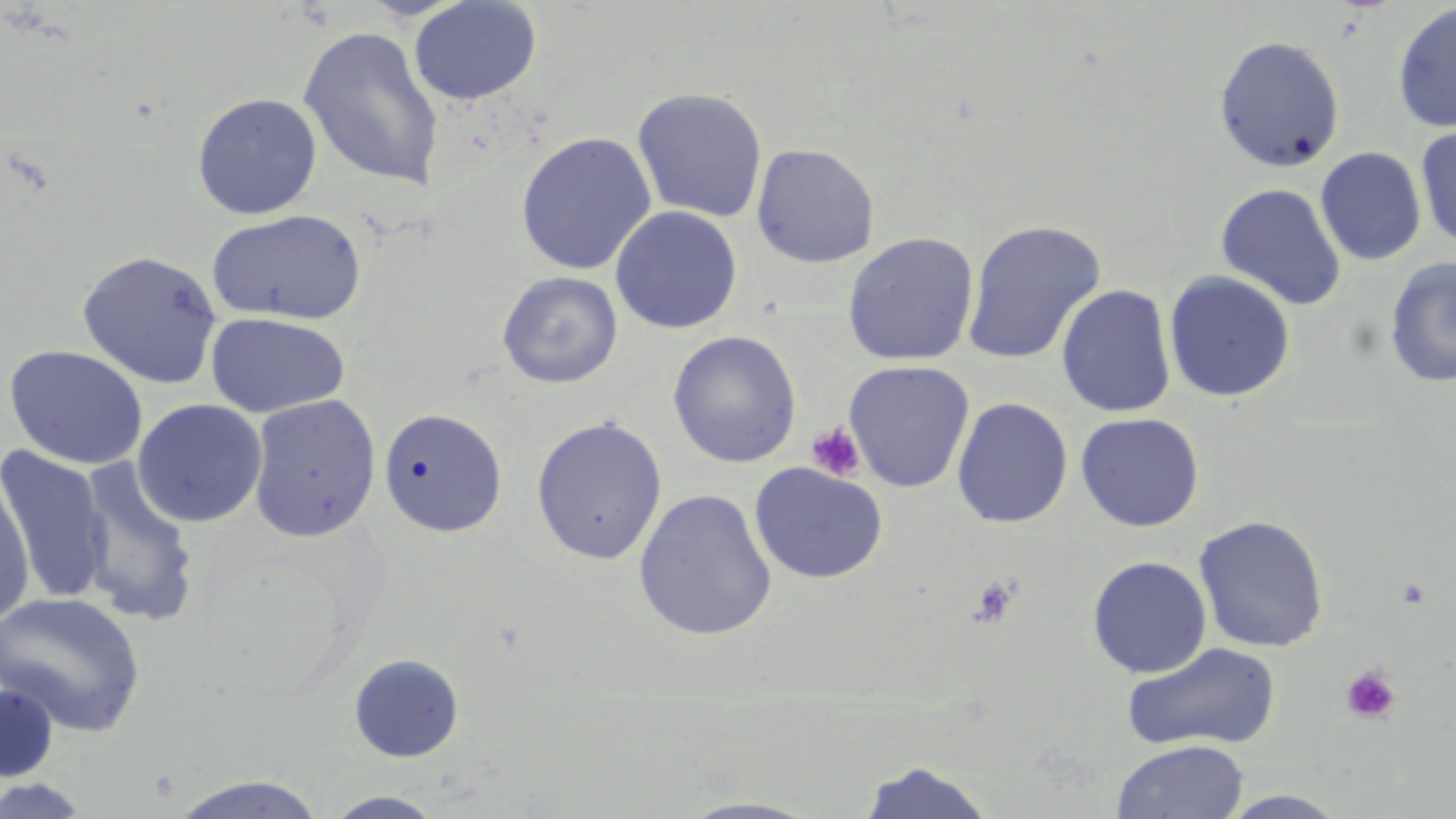

Summary:
  - Coordinate format: approximate bounding boxes as named x1/y1/x2/y2 corners in pixels
  - Uninfected red blood cell locations: (x1=409, y1=0, x2=541, y2=105), (x1=1392, y1=3, x2=1456, y2=134), (x1=297, y1=26, x2=445, y2=192), (x1=1214, y1=35, x2=1345, y2=172), (x1=632, y1=87, x2=768, y2=223), (x1=192, y1=93, x2=322, y2=219), (x1=1414, y1=124, x2=1456, y2=249), (x1=516, y1=132, x2=656, y2=275), (x1=751, y1=143, x2=880, y2=268), (x1=1315, y1=147, x2=1426, y2=266), (x1=1215, y1=182, x2=1346, y2=310), (x1=610, y1=206, x2=742, y2=333), (x1=207, y1=210, x2=367, y2=326), (x1=961, y1=219, x2=1107, y2=365), (x1=842, y1=232, x2=980, y2=365), (x1=77, y1=250, x2=223, y2=389), (x1=1385, y1=256, x2=1456, y2=387), (x1=1164, y1=270, x2=1296, y2=402), (x1=496, y1=271, x2=623, y2=388), (x1=1057, y1=284, x2=1176, y2=418), (x1=205, y1=313, x2=350, y2=417), (x1=667, y1=331, x2=802, y2=467), (x1=4, y1=345, x2=149, y2=469), (x1=843, y1=360, x2=975, y2=493), (x1=247, y1=394, x2=381, y2=542), (x1=952, y1=397, x2=1073, y2=528), (x1=132, y1=399, x2=268, y2=527), (x1=379, y1=407, x2=508, y2=537), (x1=1076, y1=412, x2=1205, y2=532), (x1=530, y1=416, x2=668, y2=565), (x1=0, y1=446, x2=113, y2=606), (x1=73, y1=458, x2=202, y2=627), (x1=749, y1=462, x2=888, y2=584), (x1=0, y1=475, x2=36, y2=626), (x1=633, y1=488, x2=777, y2=641), (x1=1193, y1=515, x2=1330, y2=652), (x1=1087, y1=555, x2=1212, y2=678), (x1=0, y1=591, x2=145, y2=737), (x1=1122, y1=641, x2=1282, y2=752), (x1=348, y1=653, x2=464, y2=763), (x1=0, y1=681, x2=59, y2=783), (x1=1111, y1=739, x2=1249, y2=819), (x1=856, y1=758, x2=998, y2=819), (x1=167, y1=774, x2=330, y2=818), (x1=0, y1=777, x2=94, y2=818), (x1=1218, y1=789, x2=1351, y2=818), (x1=323, y1=791, x2=446, y2=819), (x1=676, y1=796, x2=828, y2=818)
  - Platelet locations: (x1=807, y1=422, x2=866, y2=482), (x1=966, y1=574, x2=1022, y2=628), (x1=1395, y1=575, x2=1434, y2=610), (x1=1340, y1=666, x2=1401, y2=724)
  - Slide-level diagnosis: negative for blood parasites
  - Magnification: 1000x
  - Modality: optical microscopy
  - Field of view: one of a larger specimen
  - Preparation: thin blood film
  - Stain: May-Grünwald-Giemsa
  - Image size: 1456×819 pixels